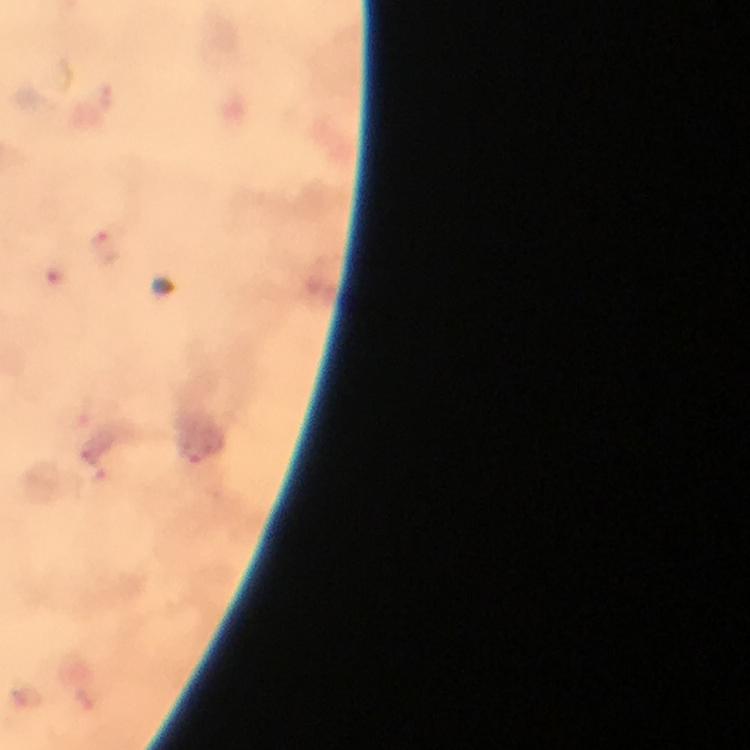

Approximate centers as {x, y} in pixels. Malaria parasite locations: {105, 248}, {194, 451}, {102, 478}. Photographed through the microscope with a smartphone camera. A crop from one field of view. Thick blood smear. At 100x magnification. Giemsa stain. From a malaria diagnostic workup. Image is 750×750 pixels. Immersion oil applied.